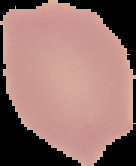

Summary:
  - Malaria status: uninfected
  - Image type: segmented cell region on a black background
  - Image size: 136×166 pixels
  - Preparation: thin blood smear